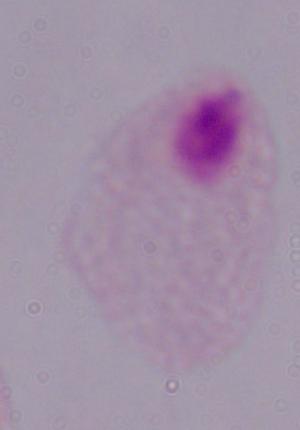 Micrograph. A trichomonad is shown. 1000x magnification.